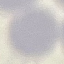

malaria status = uninfected
stain = Giemsa
capture = smartphone through the microscope eyepiece
preparation = thin smear
image type = automatically extracted cell patch, resized to 64 × 64 pixels